Assess this cell for malaria.
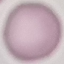
Uninfected.

Acquired by smartphone through the microscope eyepiece. Thin smear of blood. Giemsa stain. Automatically extracted cell patch, resized to 64 × 64 pixels.